Identify the preparation type.
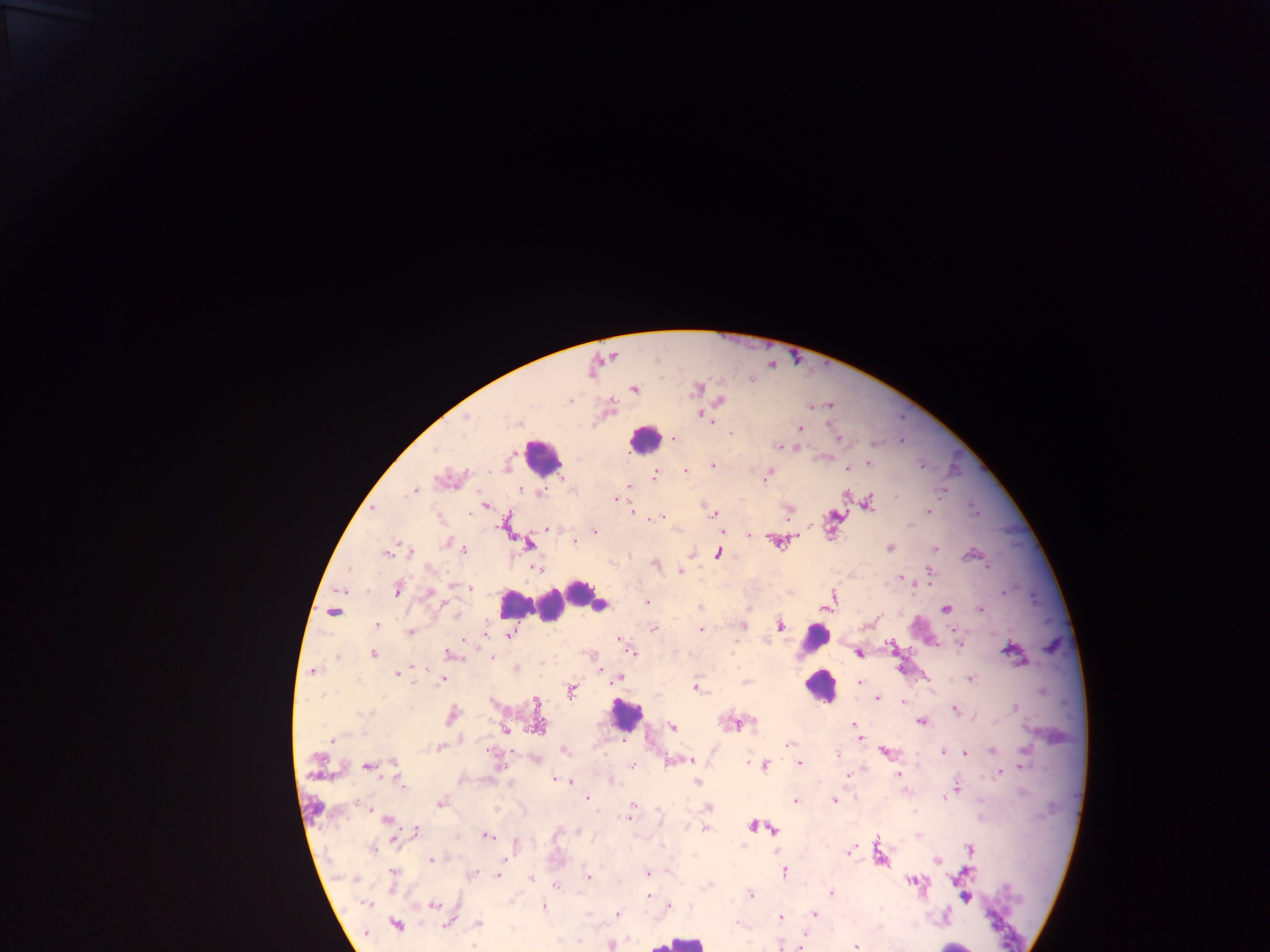
Thick blood smear.

Approximate centers as {x, y} in pixels. Leukocyte locations (subset; some below the resolvable size): {644, 439}, {542, 457}, {585, 595}, {512, 603}, {550, 607}, {333, 612}, {814, 640}, {819, 687}, {625, 715}, {678, 941}, {951, 947}. Malaria parasite locations: {634, 389}, {697, 389}, {720, 401}, {568, 402}, {829, 405}, {702, 414}, {466, 419}, {711, 422}, {800, 428}, {730, 434}, {675, 438}, {839, 439}, {778, 446}, {797, 447}, {869, 463}, {712, 465}, {847, 468}, {685, 471}, {654, 476}, {767, 476}, {629, 487}, {520, 489}, {414, 491}, {542, 492}, {895, 497}, {615, 499}, {868, 503}, {485, 505}, {373, 509}, {631, 510}, {928, 511}, {714, 514}, {661, 517}, {548, 529}, {721, 530}, {595, 532}, {751, 536}, {575, 541}, {446, 543}, {528, 543}, {890, 548}, {463, 549}, {935, 549}, {411, 552}, {387, 553}, {692, 553}, {717, 554}, {656, 564}, {432, 568}, {538, 569}, {680, 571}, {902, 578}, {929, 582}, {455, 585}, {469, 588}, {398, 590}, {430, 592}, {1004, 593}, {647, 602}, {700, 607}, {826, 608}, {947, 609}, {980, 609}, {455, 613}, {376, 625}, {744, 626}, {781, 626}, {654, 628}, {700, 630}, {410, 632}, {510, 635}, {464, 640}, {620, 640}, {959, 645}, {632, 652}, {859, 653}, {373, 654}, {450, 654}, {491, 657}, {313, 672}, {398, 674}, {442, 678}, {971, 679}, {614, 680}, {860, 682}, {696, 688}, {572, 691}, {878, 698}, {903, 702}, {536, 703}, {1015, 707}, {954, 708}, {362, 713}, {452, 716}, {921, 722}, {737, 723}, {539, 724}, {853, 725}, {672, 726}, {504, 730}, {332, 739}, {859, 739}, {788, 745}, {440, 747}, {565, 750}, {991, 750}, {943, 751}, {885, 752}, {965, 753}, {837, 754}, {689, 761}, {673, 762}, {393, 763}, {799, 763}, {765, 765}, {367, 766}, {631, 766}, {1022, 766}, {999, 773}, {397, 774}, {898, 775}, {847, 776}, {557, 780}, {401, 782}, {571, 782}, {697, 782}, {944, 797}, {588, 798}, {834, 800}, {795, 801}, {440, 803}, {634, 804}, {709, 807}, {628, 817}, {386, 819}, {752, 827}, {705, 829}, {774, 830}, {416, 832}, {487, 835}, {516, 844}, {969, 848}, {373, 849}, {850, 851}, {433, 858}, {937, 861}, {785, 872}, {499, 873}, {647, 873}, {473, 874}, {393, 875}, {588, 877}, {531, 878}, {913, 882}, {555, 886}, {831, 892}, {750, 894}, {649, 895}, {966, 897}, {366, 904}, {433, 905}, {670, 906}, {543, 908}, {617, 913}, {814, 914}, {781, 918}, {736, 922}, {396, 924}, {479, 924}, {446, 925}, {805, 936}, {611, 945}, {474, 946}, {856, 947}. Photographed through a microscope with a mobile-phone camera. Image is 1270×952 pixels. Sample from Ghana. Single field of view.